Describe the morphology of the erythrocytes.
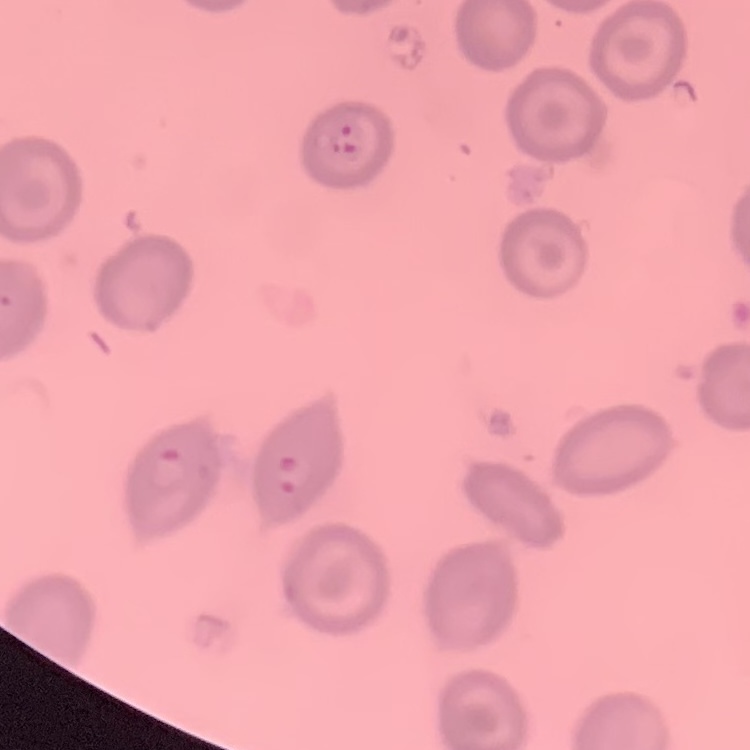

No rouleaux formation.

Summary:
  - Stain: Field's or Giemsa
  - Preparation: thin peripheral smear
  - Image type: one tile cut from a larger photomicrograph